Identify the preparation type.
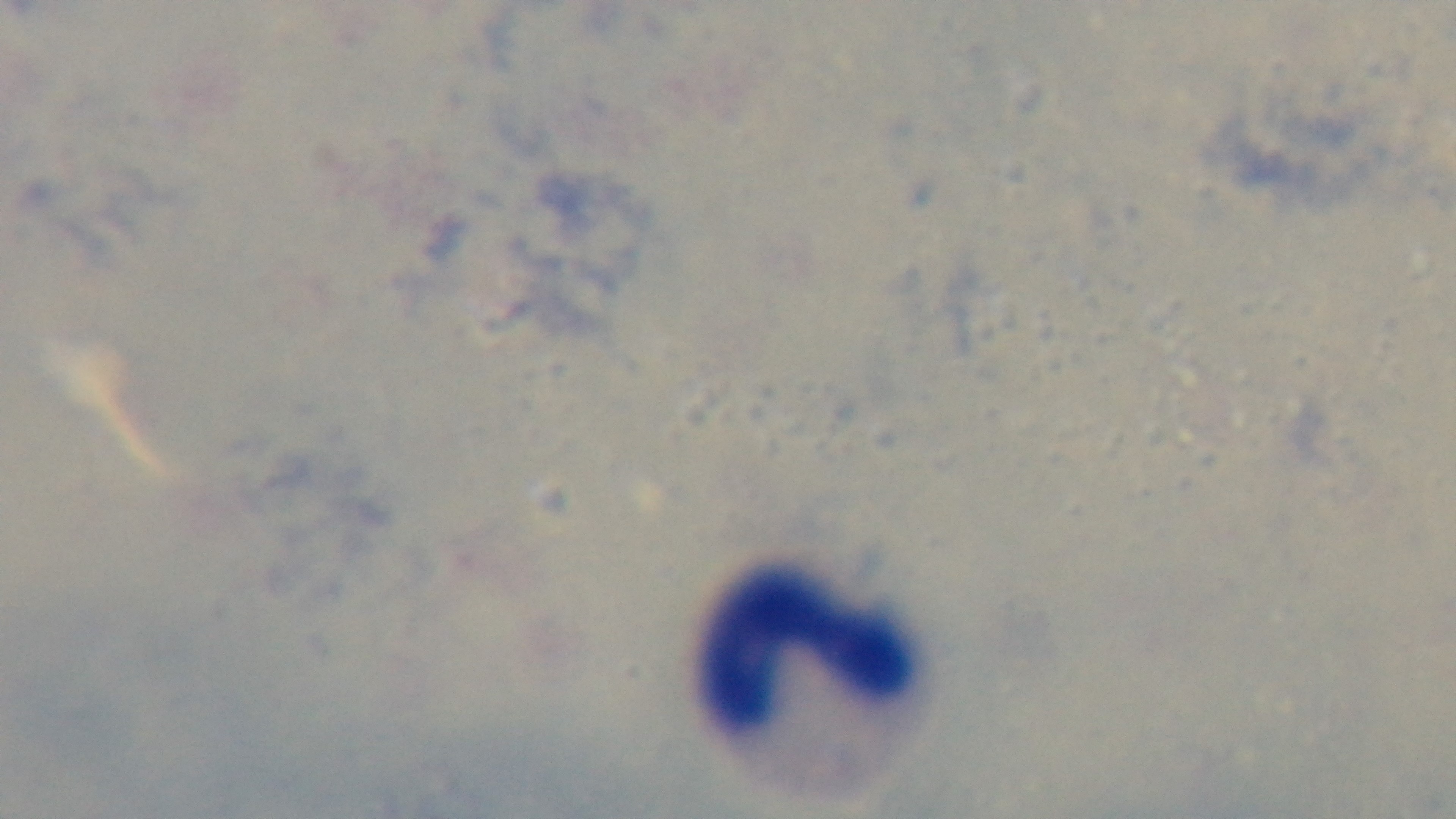
A thick smear.

field of view = one from the slide
modality = light microscopy
capture = mounted 4K digital camera
objective = 100x oil immersion
stain = Giemsa
malaria status = negative